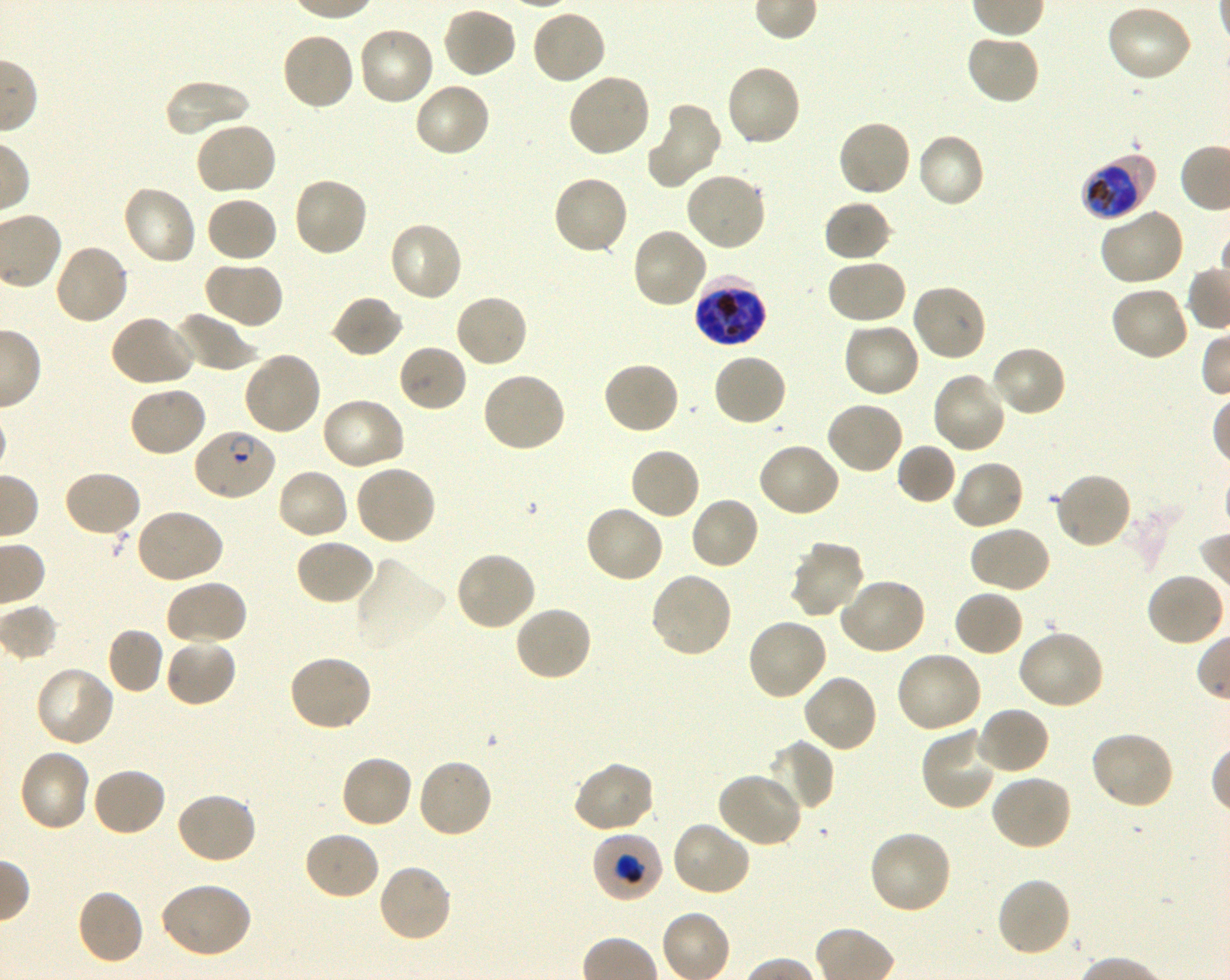

Approximate bounding boxes as (x1, y1, x2, y2) in pixels. Not every red blood cell is marked. A life-cycle stage — or a range of stages, where the recorded stages span more than one — follows each staged infected red blood cell.
Summary:
  - Locations of red blood cells of indeterminate infection status: (354, 556, 448, 653), (592, 831, 665, 903)
  - Locations of infected red blood cells: (1081, 156, 1152, 220) early trophozoite to early schizont; (695, 276, 766, 347) late trophozoite to late schizont; (192, 427, 278, 502) ring
  - Locations of uninfected red blood cells: (1105, 4, 1194, 83), (441, 5, 518, 80), (530, 7, 608, 85), (356, 24, 436, 107), (280, 32, 356, 112), (965, 34, 1042, 106), (724, 63, 802, 148), (566, 72, 652, 159), (162, 80, 253, 137), (413, 82, 493, 159), (646, 104, 722, 190), (836, 119, 912, 199), (194, 121, 279, 197), (915, 131, 986, 210), (683, 170, 767, 252), (551, 174, 631, 257), (291, 176, 369, 258), (121, 184, 198, 267), (205, 195, 279, 264), (822, 199, 893, 263), (1097, 208, 1184, 288), (388, 220, 465, 303), (631, 228, 709, 310), (54, 243, 131, 326), (825, 257, 908, 325), (201, 260, 284, 330), (910, 282, 987, 362), (1109, 286, 1191, 363), (453, 292, 530, 369), (329, 294, 404, 359), (172, 311, 257, 373), (109, 315, 197, 389), (842, 321, 922, 398), (397, 343, 468, 413), (990, 344, 1068, 418), (242, 351, 322, 437), (712, 352, 787, 428), (602, 360, 681, 435), (480, 371, 566, 454), (931, 371, 1007, 455), (127, 386, 208, 459), (320, 396, 406, 472), (825, 400, 905, 474), (756, 442, 841, 519), (896, 443, 957, 505), (628, 446, 702, 521), (951, 459, 1024, 531), (354, 463, 437, 546), (275, 467, 350, 542), (62, 469, 142, 538), (1052, 471, 1133, 550), (688, 496, 760, 572), (583, 504, 665, 584), (134, 507, 225, 585), (968, 524, 1051, 595), (294, 538, 376, 607), (788, 539, 867, 620), (454, 551, 536, 633), (648, 571, 733, 659), (1145, 574, 1225, 647), (837, 577, 927, 656), (165, 579, 248, 647), (952, 588, 1024, 657), (513, 604, 594, 682), (746, 617, 829, 702), (106, 627, 164, 694), (1016, 629, 1105, 710), (164, 638, 238, 708), (894, 650, 984, 734), (287, 653, 373, 732), (34, 666, 115, 748), (801, 672, 878, 753), (974, 706, 1051, 776), (920, 726, 998, 811), (1089, 729, 1175, 809), (764, 738, 836, 813), (17, 747, 92, 832), (339, 753, 415, 829), (416, 758, 494, 839), (572, 761, 655, 834), (91, 766, 168, 838), (716, 770, 802, 848), (990, 774, 1073, 852), (175, 791, 258, 865), (671, 821, 751, 897), (867, 829, 954, 915), (303, 831, 381, 901), (376, 863, 454, 945), (994, 876, 1073, 958), (158, 881, 254, 960), (75, 887, 146, 966)
  - Preparation: thin blood smear
  - Objective: 100x, oil immersion, numerical aperture 1.30
  - Field of view: one from this slide
  - Culture: Plasmodium falciparum strain 3D7, shaking, in vitro
  - Donor blood group: O+
  - Stain: Giemsa
  - Image size: 1230×980 pixels